Assess this cell for malaria.
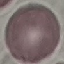
It is uninfected.

capture = smartphone through the microscope eyepiece
image type = automatically extracted cell patch, resized to 64 × 64 pixels
preparation = thin smear
stain = Giemsa